Locate and identify every blood parasite.
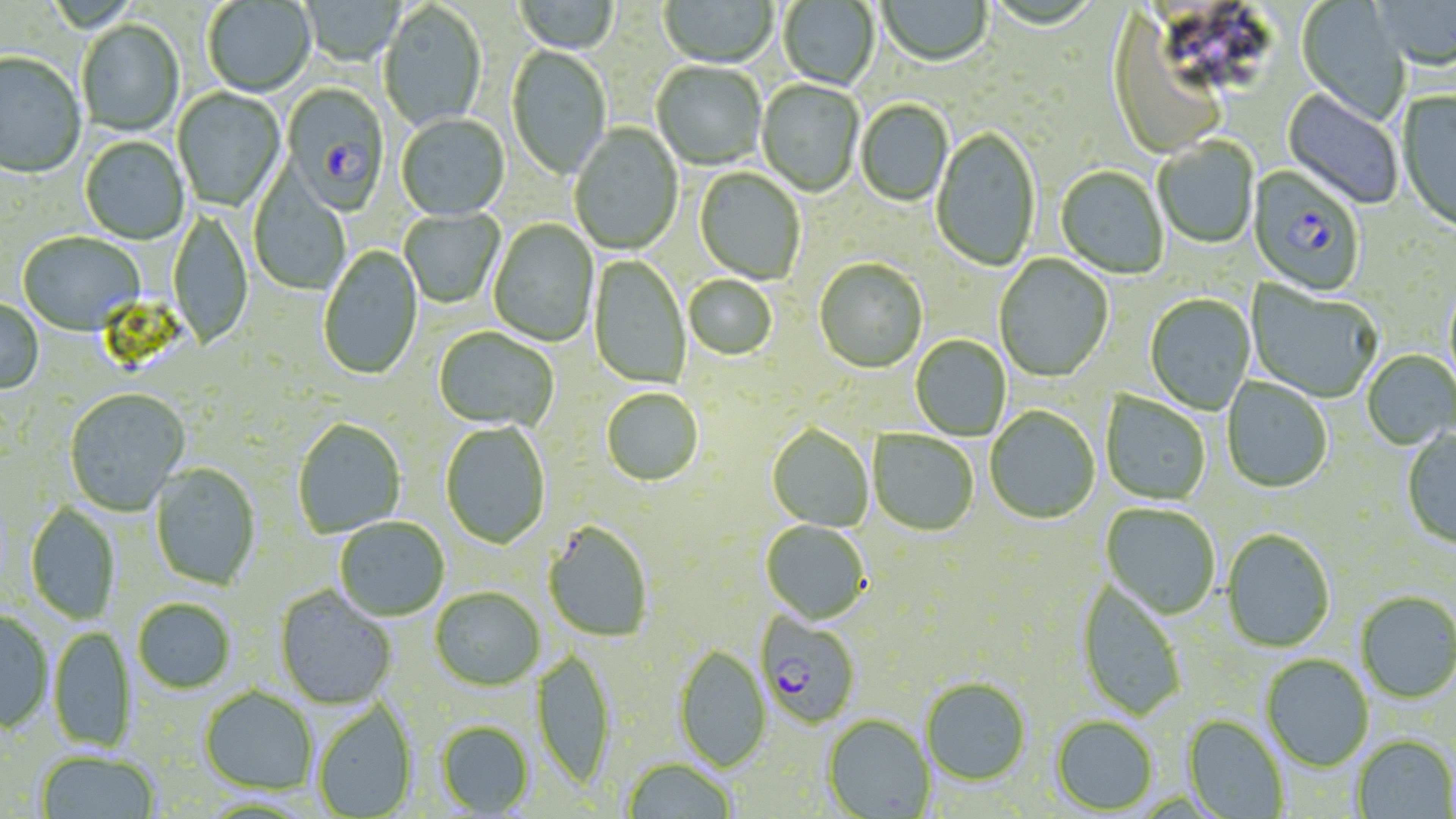
Approximate bounding boxes as (x1, y1, x2, y2) in pixels.
Plasmodium falciparum-infected red blood cells: (282, 85, 390, 215), (1246, 167, 1365, 297), (756, 612, 862, 728).
No Plasmodium ovale, Plasmodium malariae, Plasmodium vivax, Babesia divergens, or Trypanosoma brucei observed.

Uninfected red blood cell locations: (514, 0, 620, 54), (659, 0, 778, 70), (778, 0, 880, 92), (878, 0, 992, 68), (1372, 0, 1456, 72), (203, 1, 316, 97), (301, 1, 406, 67), (1296, 1, 1410, 124), (379, 3, 486, 133), (1107, 7, 1228, 167), (77, 21, 184, 137), (506, 46, 611, 183), (0, 54, 86, 179), (652, 61, 766, 171), (757, 80, 863, 198), (173, 88, 286, 212), (1282, 88, 1403, 210), (1396, 90, 1456, 234), (855, 100, 953, 207), (396, 115, 510, 222), (569, 123, 683, 256), (932, 128, 1040, 272), (80, 137, 189, 245), (1154, 137, 1259, 249), (1055, 167, 1168, 280), (694, 168, 805, 284), (249, 172, 349, 295), (168, 207, 253, 351), (399, 209, 504, 309), (489, 219, 599, 347), (18, 232, 144, 336), (317, 245, 424, 380), (994, 254, 1113, 383), (589, 255, 691, 390), (814, 259, 928, 373), (683, 276, 777, 360), (1246, 281, 1382, 403), (1145, 294, 1256, 415), (0, 298, 44, 395), (433, 327, 558, 431), (910, 335, 1011, 441), (1362, 350, 1455, 450), (1222, 377, 1333, 493), (64, 388, 190, 515), (601, 388, 703, 486), (1100, 392, 1210, 506), (985, 406, 1100, 525), (293, 418, 407, 537), (440, 422, 551, 549), (767, 424, 874, 532), (1402, 429, 1456, 550), (868, 431, 978, 536), (151, 463, 261, 591), (25, 502, 120, 624), (1101, 504, 1221, 620), (335, 517, 450, 621), (543, 520, 654, 642), (761, 520, 871, 624), (1221, 529, 1335, 652), (1076, 579, 1187, 720), (274, 587, 397, 708), (430, 587, 545, 690), (1355, 591, 1456, 703), (132, 598, 236, 693), (0, 610, 54, 733), (49, 625, 136, 752), (674, 646, 770, 771), (532, 649, 616, 788), (1261, 654, 1374, 771), (921, 678, 1030, 784), (200, 686, 318, 795), (314, 698, 418, 818), (822, 715, 936, 818), (1184, 715, 1289, 818), (1052, 716, 1158, 814), (435, 720, 535, 816), (1352, 735, 1455, 818), (35, 749, 160, 818), (622, 758, 737, 818). Slide-level diagnosis: Plasmodium falciparum. 1000x magnification. May-Grünwald-Giemsa-stained preparation. Light microscopy. Image is 1456×819 pixels. Thin blood film. Single field of view.